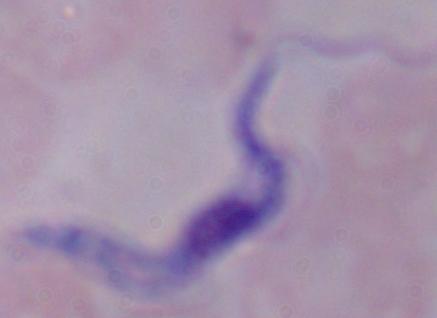
identification = trypanosome
magnification = 1000x
modality = photomicrograph